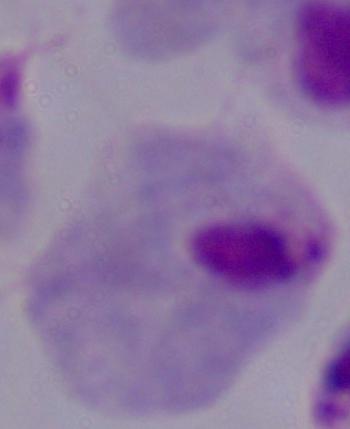

identification: trichomonad
magnification: 1000x
modality: micrograph